Mark where platelets are.
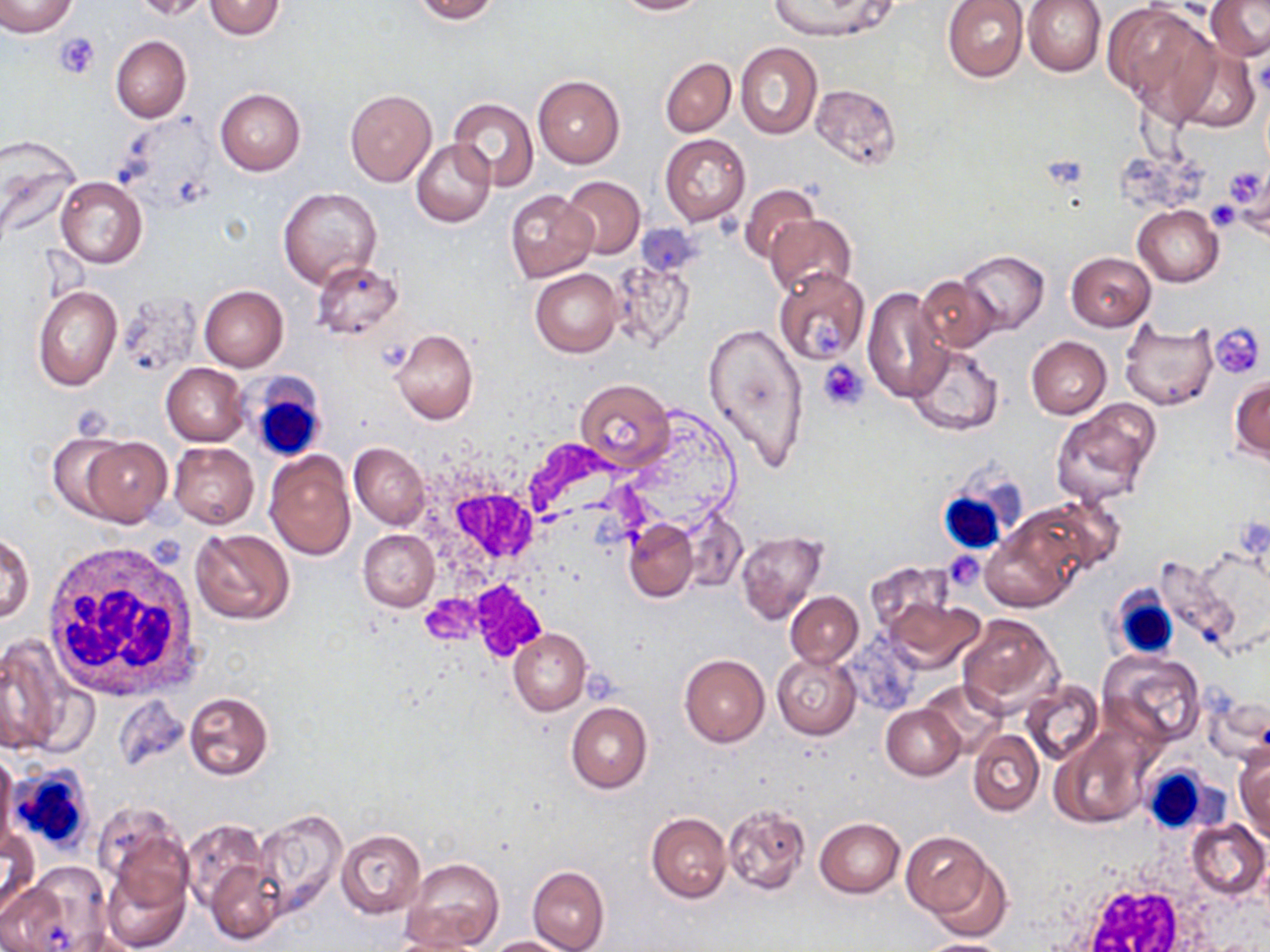
Approximate bounding boxes as (x1,y1)-(x2,y2) corner pairs in pixels.
Platelets: (55,32)-(100,79), (1223,167)-(1268,206), (1208,200)-(1243,232), (806,316)-(839,355), (1210,323)-(1266,379), (819,360)-(867,410), (149,534)-(186,570), (948,550)-(981,590).

Summary:
  - Uninfected red blood cell locations: (0,0)-(78,39), (133,0)-(211,20), (205,0)-(285,39), (410,0)-(498,23), (612,0)-(708,15), (943,0)-(1029,80), (1023,0)-(1106,77), (1205,0)-(1270,62), (767,1)-(900,43), (1103,4)-(1213,113), (111,35)-(191,122), (735,43)-(822,140), (1172,46)-(1258,134), (660,58)-(736,136), (533,75)-(624,168), (812,85)-(899,169), (215,87)-(305,176), (346,88)-(436,185), (449,98)-(537,189), (660,135)-(750,224), (0,139)-(81,251), (412,139)-(496,228), (54,176)-(147,269), (560,176)-(645,259), (739,183)-(821,266), (277,186)-(382,289), (505,190)-(596,282), (1134,205)-(1223,286), (765,214)-(857,296), (609,250)-(694,349), (958,250)-(1048,334), (1065,252)-(1156,331), (310,259)-(402,341), (530,268)-(622,357), (773,268)-(870,365), (916,276)-(1000,352), (199,285)-(288,372), (862,285)-(953,404), (33,286)-(122,391), (1120,318)-(1218,410), (701,321)-(809,473), (390,329)-(478,425), (1026,336)-(1111,418), (906,344)-(1004,436), (162,363)-(248,446), (1230,377)-(1270,460), (575,378)-(673,470), (1050,400)-(1159,506), (48,433)-(136,521), (80,437)-(172,526), (169,442)-(258,529), (350,442)-(431,528), (264,451)-(355,558), (1027,496)-(1124,577), (678,506)-(748,593), (623,517)-(698,602), (982,523)-(1079,611), (191,528)-(295,626), (1,530)-(33,626), (359,530)-(439,610), (735,531)-(829,625), (1154,555)-(1250,653), (864,562)-(954,638), (785,591)-(863,667), (883,597)-(984,675), (956,614)-(1062,717), (509,629)-(591,716), (0,637)-(71,754), (1101,651)-(1205,747), (772,653)-(861,738), (680,655)-(770,748), (919,680)-(1006,756), (1022,681)-(1104,767), (183,690)-(273,781), (114,694)-(188,772), (566,702)-(651,794), (882,705)-(965,780), (968,729)-(1044,816), (1052,730)-(1148,828), (1235,749)-(1270,842), (0,752)-(17,852), (93,803)-(188,903), (722,803)-(809,895), (251,809)-(347,920), (646,812)-(732,903), (815,818)-(904,897), (1187,819)-(1268,899), (180,820)-(269,912), (1,827)-(39,914), (336,829)-(424,917), (901,830)-(997,919), (923,852)-(1013,940), (206,858)-(286,944), (403,858)-(504,951), (100,860)-(191,951), (18,862)-(110,948), (528,866)-(608,952), (0,879)-(77,952), (384,934)-(483,952), (486,935)-(570,952), (914,937)-(1013,952)
  - White blood cell locations: (247,379)-(328,465), (425,440)-(604,656), (938,461)-(1030,550), (42,543)-(201,702), (1110,587)-(1179,661), (5,764)-(97,858), (1141,764)-(1212,831)
  - Slide-level diagnosis: no evidence of blood parasites
  - Image size: 1270×952 pixels
  - Field of view: one of a larger specimen
  - Modality: light microscopy
  - Preparation: thin blood smear
  - Stain: May-Grünwald-Giemsa
  - Magnification: 1000x